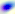 Photomicrograph. Toxoplasma gondii is shown. 400x magnification.